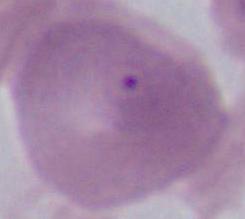 1000x magnification. Micrograph. A red blood cell is shown.